Comment on the morphology of the red blood cells.
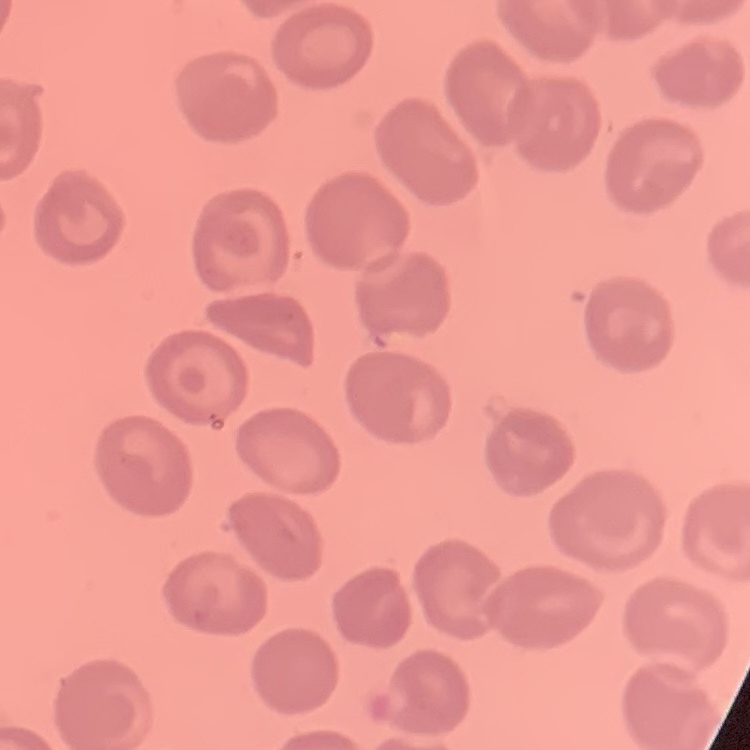
No rouleaux formation.

Summary:
  - Preparation: thin blood smear
  - Image type: square crop of a larger photomicrograph
  - Stain: Field's or Giemsa